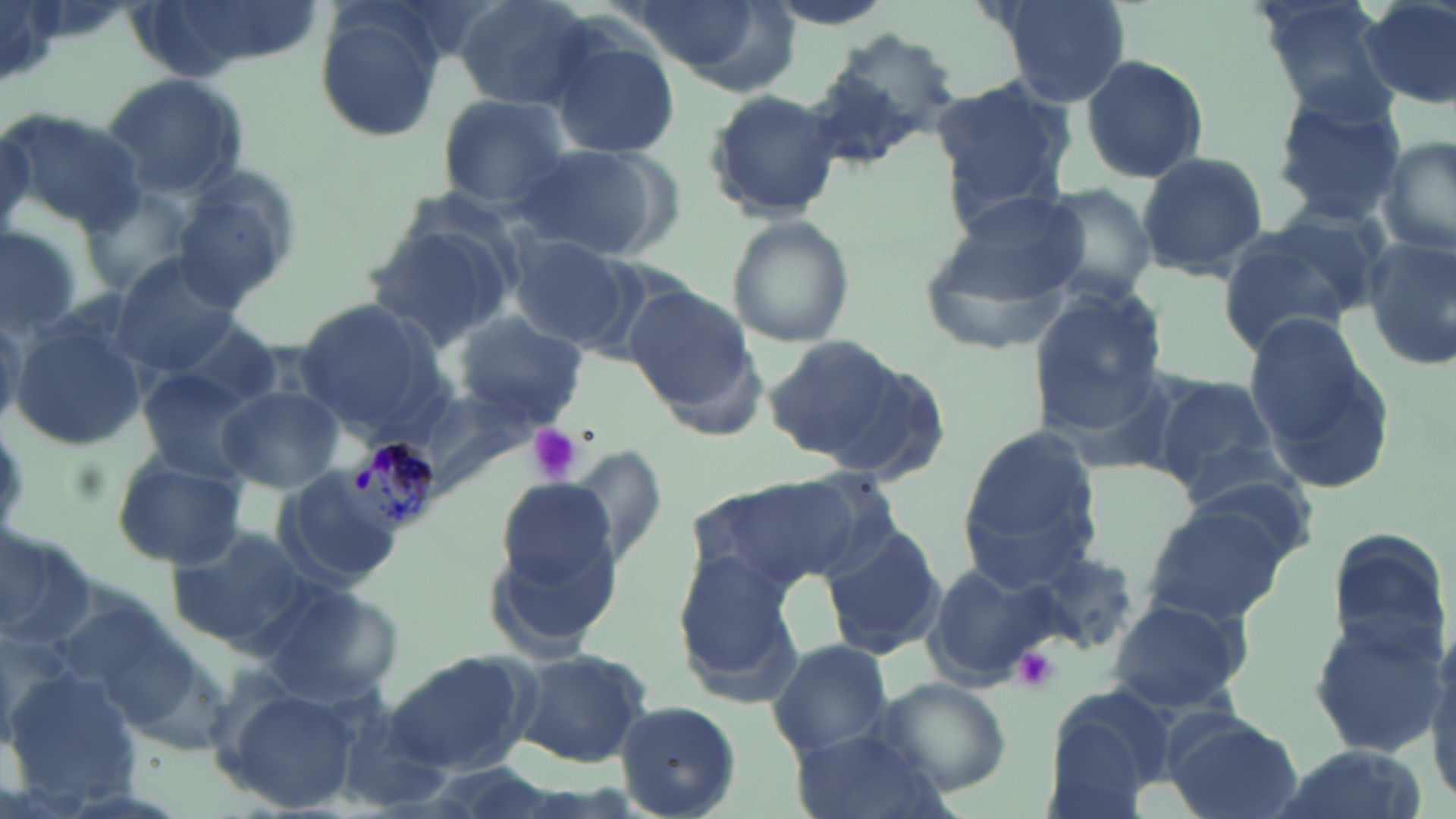
slide-level diagnosis = Plasmodium malariae
magnification = 1000x
preparation = thin blood film
modality = optical microscopy
stain = May-Grünwald-Giemsa
platelet locations = approximate bounding boxes as named x1/y1/x2/y2 corners in pixels: (x1=526, y1=424, x2=581, y2=483), (x1=1013, y1=647, x2=1059, y2=691)
Plasmodium malariae-infected red blood cell locations = approximate bounding boxes as named x1/y1/x2/y2 corners in pixels: (x1=344, y1=438, x2=444, y2=537)
image size = 1456×819 pixels
uninfected red blood cell locations = approximate bounding boxes as named x1/y1/x2/y2 corners in pixels: (x1=454, y1=0, x2=598, y2=111), (x1=758, y1=0, x2=898, y2=30), (x1=990, y1=0, x2=1131, y2=104), (x1=1253, y1=0, x2=1401, y2=117), (x1=1359, y1=0, x2=1456, y2=107), (x1=2, y1=2, x2=61, y2=90), (x1=313, y1=6, x2=444, y2=141), (x1=820, y1=31, x2=958, y2=149), (x1=548, y1=34, x2=681, y2=161), (x1=1080, y1=55, x2=1210, y2=184), (x1=101, y1=72, x2=248, y2=199), (x1=932, y1=74, x2=1076, y2=214), (x1=1267, y1=86, x2=1409, y2=222), (x1=704, y1=90, x2=845, y2=220), (x1=437, y1=94, x2=572, y2=208), (x1=2, y1=108, x2=147, y2=234), (x1=0, y1=121, x2=35, y2=236), (x1=1378, y1=135, x2=1456, y2=263), (x1=510, y1=143, x2=675, y2=261), (x1=1134, y1=151, x2=1269, y2=280), (x1=171, y1=178, x2=299, y2=311), (x1=1037, y1=183, x2=1160, y2=304), (x1=83, y1=186, x2=195, y2=294), (x1=933, y1=196, x2=1087, y2=308), (x1=726, y1=216, x2=851, y2=347), (x1=0, y1=221, x2=89, y2=334), (x1=1218, y1=221, x2=1372, y2=354), (x1=364, y1=224, x2=516, y2=351), (x1=510, y1=237, x2=632, y2=347), (x1=1359, y1=237, x2=1456, y2=369), (x1=110, y1=256, x2=242, y2=376), (x1=626, y1=285, x2=755, y2=410), (x1=1029, y1=292, x2=1166, y2=424), (x1=292, y1=297, x2=444, y2=430), (x1=168, y1=311, x2=285, y2=409), (x1=452, y1=311, x2=587, y2=423), (x1=1244, y1=314, x2=1391, y2=484), (x1=0, y1=320, x2=23, y2=430), (x1=8, y1=325, x2=146, y2=452), (x1=762, y1=335, x2=901, y2=459), (x1=135, y1=369, x2=256, y2=481), (x1=1148, y1=373, x2=1281, y2=493), (x1=399, y1=379, x2=543, y2=498), (x1=216, y1=385, x2=342, y2=492), (x1=958, y1=427, x2=1102, y2=582), (x1=563, y1=449, x2=668, y2=567), (x1=109, y1=451, x2=249, y2=567), (x1=759, y1=468, x2=906, y2=583), (x1=272, y1=470, x2=404, y2=592), (x1=495, y1=478, x2=618, y2=590), (x1=683, y1=479, x2=844, y2=591), (x1=1141, y1=503, x2=1289, y2=624), (x1=0, y1=521, x2=97, y2=646), (x1=164, y1=523, x2=318, y2=650), (x1=819, y1=523, x2=946, y2=658), (x1=1323, y1=527, x2=1452, y2=657), (x1=1017, y1=544, x2=1137, y2=659), (x1=671, y1=548, x2=806, y2=702), (x1=922, y1=561, x2=1061, y2=687), (x1=249, y1=579, x2=399, y2=703), (x1=1106, y1=594, x2=1251, y2=713), (x1=1305, y1=615, x2=1447, y2=760), (x1=1424, y1=620, x2=1456, y2=812), (x1=767, y1=638, x2=893, y2=757), (x1=115, y1=643, x2=235, y2=756), (x1=511, y1=647, x2=653, y2=767), (x1=388, y1=654, x2=534, y2=775), (x1=2, y1=665, x2=139, y2=799), (x1=867, y1=674, x2=1012, y2=797), (x1=1042, y1=683, x2=1178, y2=814), (x1=224, y1=687, x2=357, y2=813), (x1=616, y1=701, x2=741, y2=817), (x1=330, y1=707, x2=452, y2=813), (x1=1162, y1=713, x2=1301, y2=819), (x1=790, y1=724, x2=944, y2=819), (x1=1262, y1=745, x2=1424, y2=819)
field of view = single